Point out each Plasmodium parasite.
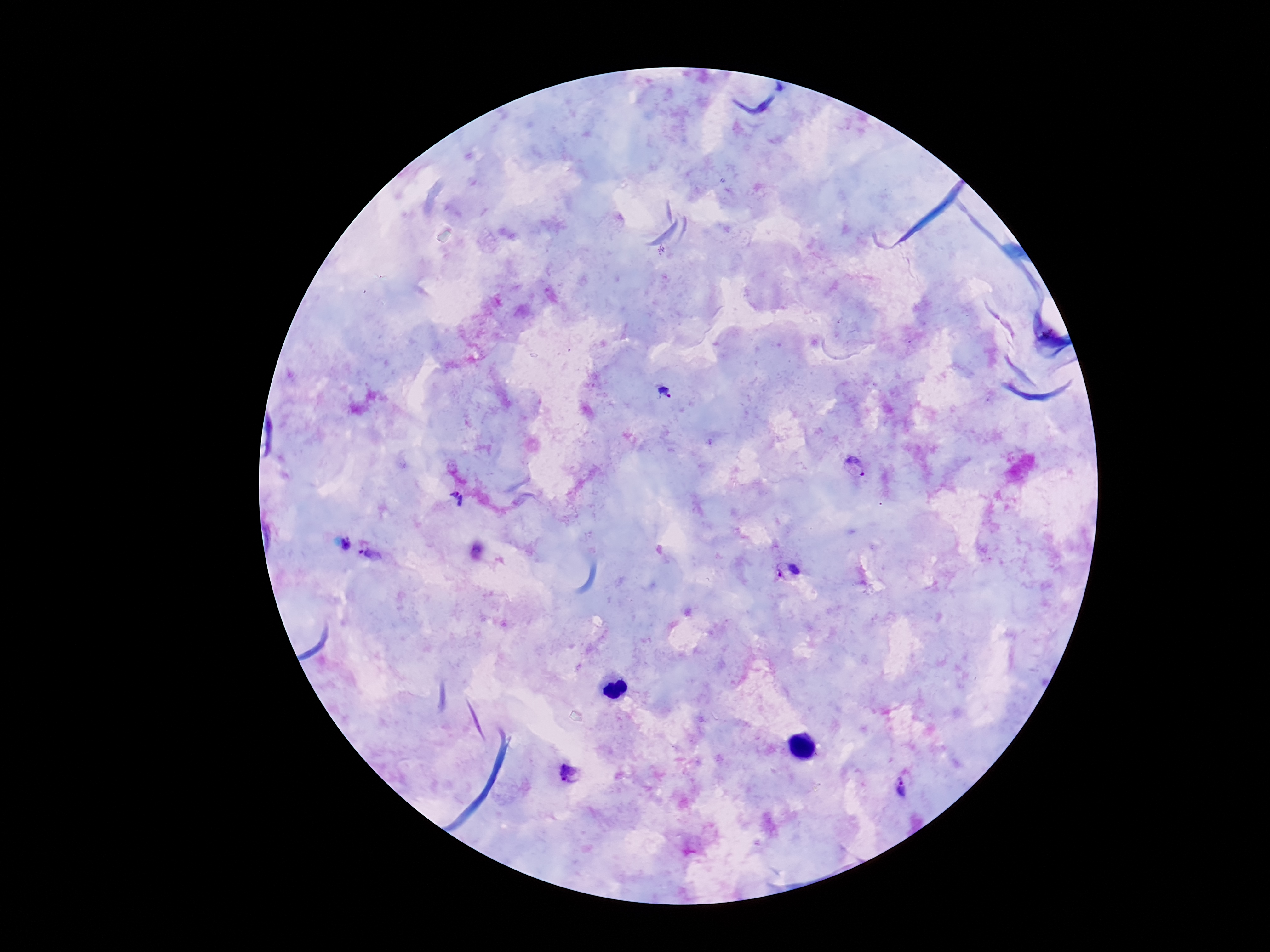
Approximate centers as (x, y) in pixels.
Plasmodium parasites: (666, 393), (855, 467), (456, 500), (347, 544), (370, 554), (787, 570), (571, 776), (903, 790).

stain = Giemsa
capture = smartphone camera through the microscope eyepiece
patient malaria status = positive
preparation = thick blood smear
image size = 1270×952 pixels
magnification = 100x
field of view = one from this slide